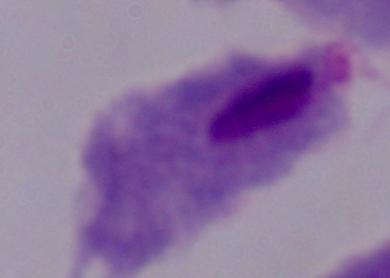
{
  "identification": "trichomonad",
  "modality": "micrograph",
  "magnification": "1000x"
}